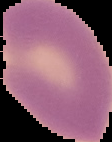

malaria status = parasitized
image type = segmented cell region on a black background
image size = 112×142 pixels
preparation = thin blood film